Assess this cell for malaria.
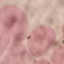

It is uninfected.

image type = cell patch, automatically extracted from a larger field of view and resized to 64 × 64 pixels
preparation = thin smear
stain = Giemsa
capture = smartphone through the microscope eyepiece